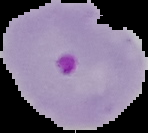

Summary:
  - Image size: 148×133 pixels
  - Result: malaria parasites detected
  - Preparation: thin blood film
  - Image type: segmented cell region on a black background